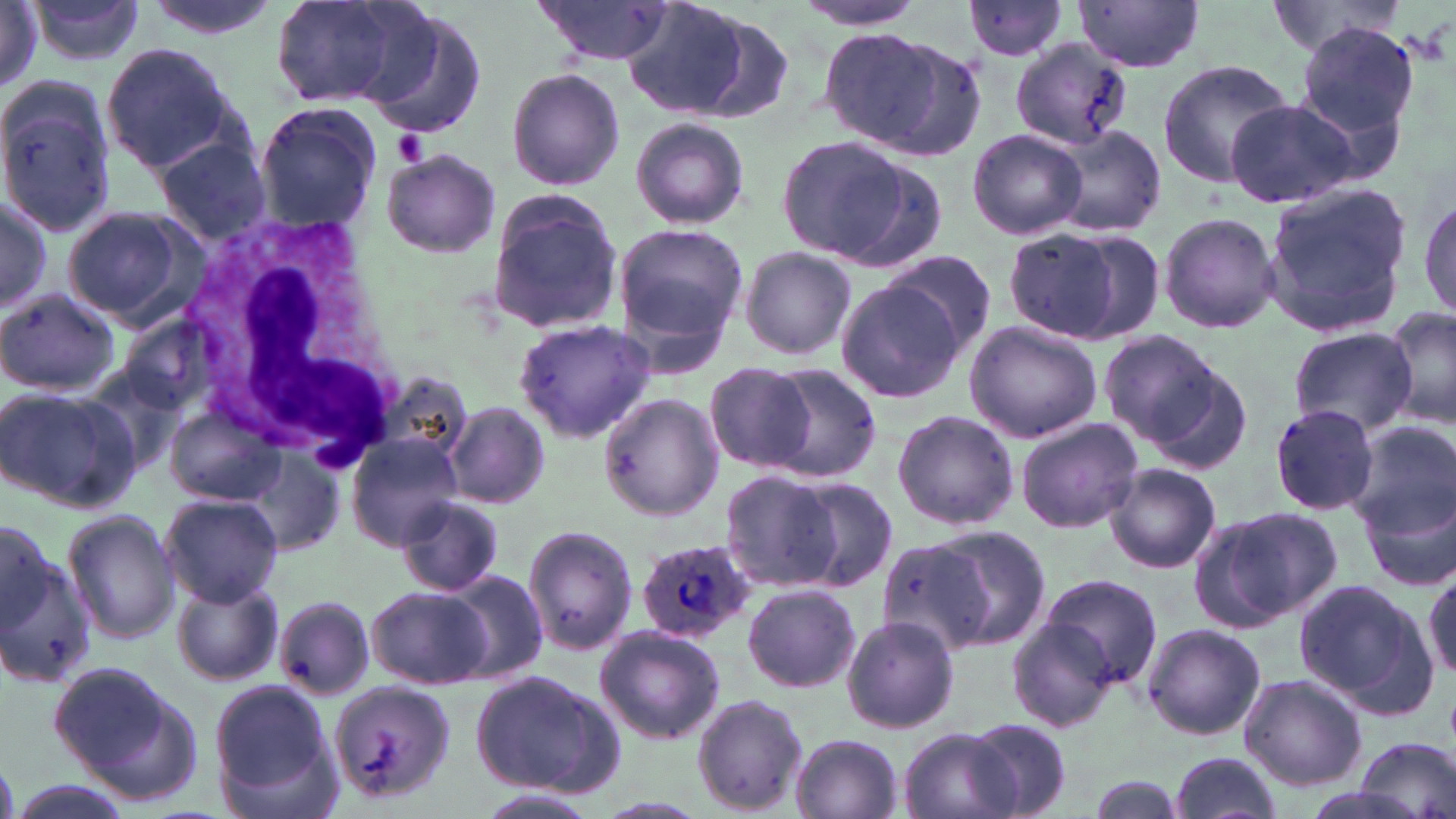
Summary:
  - Coordinate format: approximate bounding boxes as (x1, y1, x2, y2) in pixels
  - Uninfected red blood cell locations: (140, 0, 278, 41), (267, 0, 429, 110), (1261, 0, 1413, 60), (530, 1, 676, 67), (963, 1, 1071, 63), (1072, 1, 1206, 71), (26, 2, 148, 67), (622, 2, 764, 118), (789, 2, 937, 31), (1, 3, 47, 91), (360, 10, 490, 140), (678, 11, 801, 123), (1292, 20, 1422, 151), (819, 27, 981, 159), (1010, 37, 1132, 149), (101, 43, 239, 175), (1156, 58, 1296, 189), (505, 68, 626, 191), (0, 77, 118, 238), (1224, 99, 1358, 208), (254, 103, 379, 230), (630, 116, 749, 231), (1046, 126, 1169, 239), (966, 127, 1087, 243), (774, 133, 930, 267), (152, 135, 273, 245), (380, 150, 500, 258), (1260, 181, 1415, 340), (0, 191, 53, 319), (485, 191, 624, 335), (1417, 191, 1456, 325), (61, 206, 198, 327), (1156, 210, 1282, 336), (613, 222, 748, 350), (1003, 227, 1147, 345), (738, 246, 858, 360), (878, 249, 1001, 359), (833, 278, 963, 406), (0, 286, 121, 398), (1381, 304, 1456, 431), (515, 319, 658, 444), (964, 319, 1103, 442), (1286, 326, 1418, 437), (1097, 329, 1223, 447), (1135, 348, 1255, 473), (756, 362, 882, 483), (704, 363, 815, 472), (369, 369, 473, 473), (0, 385, 142, 512), (598, 392, 726, 520), (167, 402, 287, 505), (445, 402, 550, 509), (1268, 403, 1382, 517), (891, 409, 1019, 532), (1014, 416, 1142, 534), (1350, 420, 1455, 542), (346, 434, 465, 549), (1099, 461, 1223, 572), (1357, 467, 1456, 595), (718, 469, 844, 592), (788, 477, 900, 592), (159, 493, 284, 607), (394, 493, 506, 598), (1198, 506, 1341, 627), (61, 509, 181, 646), (522, 525, 638, 657), (933, 526, 1052, 649), (0, 530, 94, 689), (872, 530, 1009, 653), (439, 571, 549, 684), (1424, 571, 1456, 682), (172, 575, 283, 689), (1038, 575, 1161, 688), (1296, 579, 1440, 721), (742, 582, 861, 693), (368, 586, 490, 689), (276, 597, 374, 700), (840, 615, 960, 734), (1009, 618, 1119, 731), (1141, 623, 1266, 741), (594, 626, 726, 744), (53, 663, 203, 803), (466, 670, 626, 798), (1237, 673, 1367, 789), (211, 681, 332, 797), (328, 681, 454, 808), (691, 694, 808, 815), (965, 718, 1073, 817), (896, 728, 1019, 819), (217, 733, 347, 819), (789, 733, 903, 819), (1349, 737, 1454, 819), (1167, 752, 1284, 819), (1085, 775, 1189, 818), (5, 781, 131, 819), (479, 789, 602, 819)
  - Platelet locations: (394, 129, 429, 164)
  - Plasmodium ovale-infected red blood cell locations: (635, 538, 758, 642)
  - White blood cell locations: (181, 214, 406, 472)
  - Slide-level diagnosis: Plasmodium ovale
  - Preparation: thin blood film
  - Modality: light microscopy
  - Magnification: 1000x
  - Image size: 1456×819 pixels
  - Stain: May-Grünwald-Giemsa
  - Field of view: single